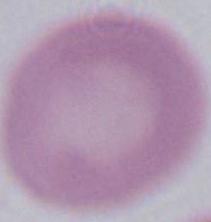

Summary:
  - Identification: red blood cell
  - Modality: micrograph
  - Magnification: 1000x